Classify this cell by malaria status.
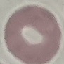

Uninfected.

stain = Giemsa
image type = automatically extracted cell patch, resized to 64 × 64 pixels
preparation = thin smear
capture = smartphone camera at the microscope eyepiece